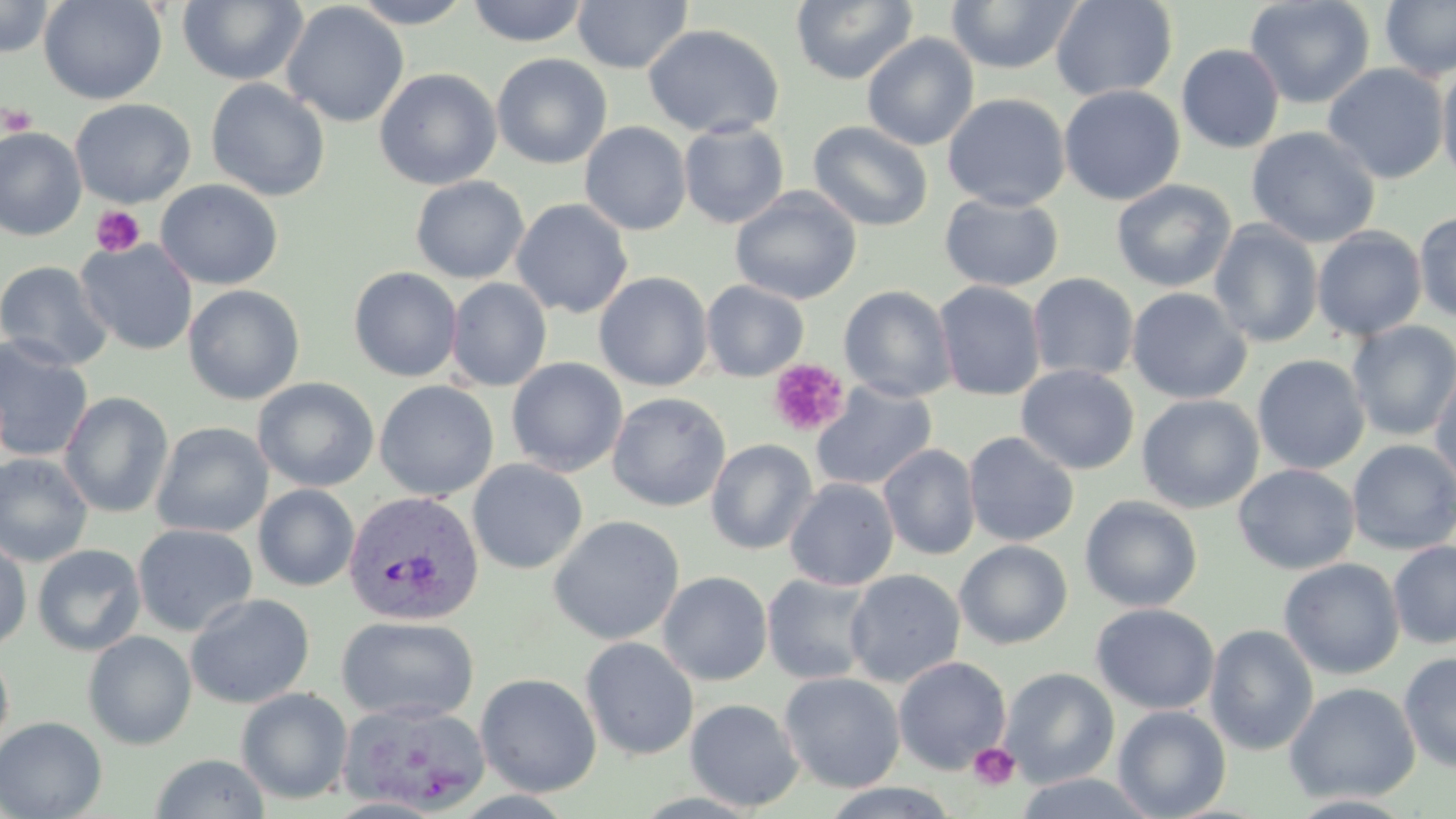
slide-level diagnosis = Plasmodium vivax
stain = May-Grünwald-Giemsa
Plasmodium vivax-infected red blood cell locations = approximate bounding boxes as [x1, y1, x2, y2] in pixels: [343, 490, 484, 627]
magnification = 1000x
preparation = thin blood smear
platelet locations = approximate bounding boxes as [x1, y1, x2, y2] in pixels: [1, 103, 37, 135], [90, 205, 146, 257], [767, 359, 850, 438], [967, 742, 1020, 790]
image size = 1456×819 pixels
field of view = one of a larger specimen
uninfected red blood cell locations = approximate bounding boxes as [x1, y1, x2, y2] in pixels: [0, 0, 57, 58], [38, 0, 167, 105], [177, 0, 308, 86], [347, 0, 476, 28], [466, 0, 588, 46], [572, 0, 692, 74], [791, 0, 918, 85], [1051, 0, 1178, 101], [1244, 0, 1375, 110], [1380, 0, 1456, 81], [946, 1, 1083, 74], [281, 2, 409, 127], [643, 23, 784, 139], [862, 32, 979, 151], [1176, 44, 1285, 154], [492, 53, 612, 170], [1437, 60, 1456, 187], [1322, 63, 1449, 184], [374, 68, 502, 190], [206, 78, 330, 201], [1059, 85, 1185, 205], [942, 93, 1070, 211], [70, 98, 196, 208], [679, 120, 789, 229], [808, 121, 934, 231], [579, 122, 691, 235], [1246, 126, 1380, 247], [0, 127, 86, 241], [410, 176, 529, 283], [155, 179, 283, 290], [1111, 179, 1237, 293], [730, 186, 862, 305], [939, 192, 1063, 292], [511, 198, 633, 318], [1413, 211, 1456, 324], [1208, 221, 1324, 348], [1312, 226, 1427, 341], [75, 238, 197, 356], [0, 260, 114, 371], [348, 266, 463, 382], [593, 271, 713, 391], [1027, 272, 1139, 383], [446, 278, 552, 392], [700, 280, 809, 381], [933, 281, 1046, 401], [183, 284, 305, 405], [839, 285, 956, 402], [1126, 287, 1252, 404], [1346, 320, 1456, 441], [0, 334, 95, 463], [1252, 354, 1370, 475], [506, 358, 628, 478], [1430, 361, 1456, 495], [1016, 365, 1139, 475], [252, 377, 379, 492], [374, 380, 499, 501], [811, 381, 937, 492], [59, 392, 174, 519], [607, 392, 731, 512], [1137, 394, 1264, 514], [151, 422, 273, 538], [963, 431, 1079, 547], [705, 438, 818, 555], [1347, 439, 1456, 555], [878, 443, 981, 561], [0, 452, 94, 568], [467, 459, 588, 575], [1233, 463, 1360, 574], [784, 478, 899, 591], [253, 484, 360, 591], [1079, 496, 1203, 613], [548, 515, 685, 645], [132, 524, 258, 636], [0, 535, 32, 653], [954, 540, 1073, 649], [1388, 540, 1456, 650], [31, 544, 147, 656], [1279, 558, 1405, 680], [844, 569, 966, 687], [658, 571, 772, 686], [762, 573, 876, 685], [185, 592, 316, 709], [1091, 602, 1219, 714], [337, 615, 480, 723], [1204, 624, 1320, 757], [83, 631, 197, 750], [580, 636, 699, 760], [0, 646, 14, 756], [1398, 651, 1456, 774], [893, 656, 1011, 775], [999, 667, 1120, 788], [779, 671, 905, 793], [475, 672, 602, 797], [1284, 682, 1421, 804], [237, 687, 353, 805], [685, 698, 803, 812], [338, 699, 491, 815], [1113, 705, 1231, 819], [0, 716, 107, 819], [149, 753, 269, 819], [1012, 771, 1159, 818], [816, 782, 964, 819], [1285, 793, 1422, 817]
modality = light microscopy